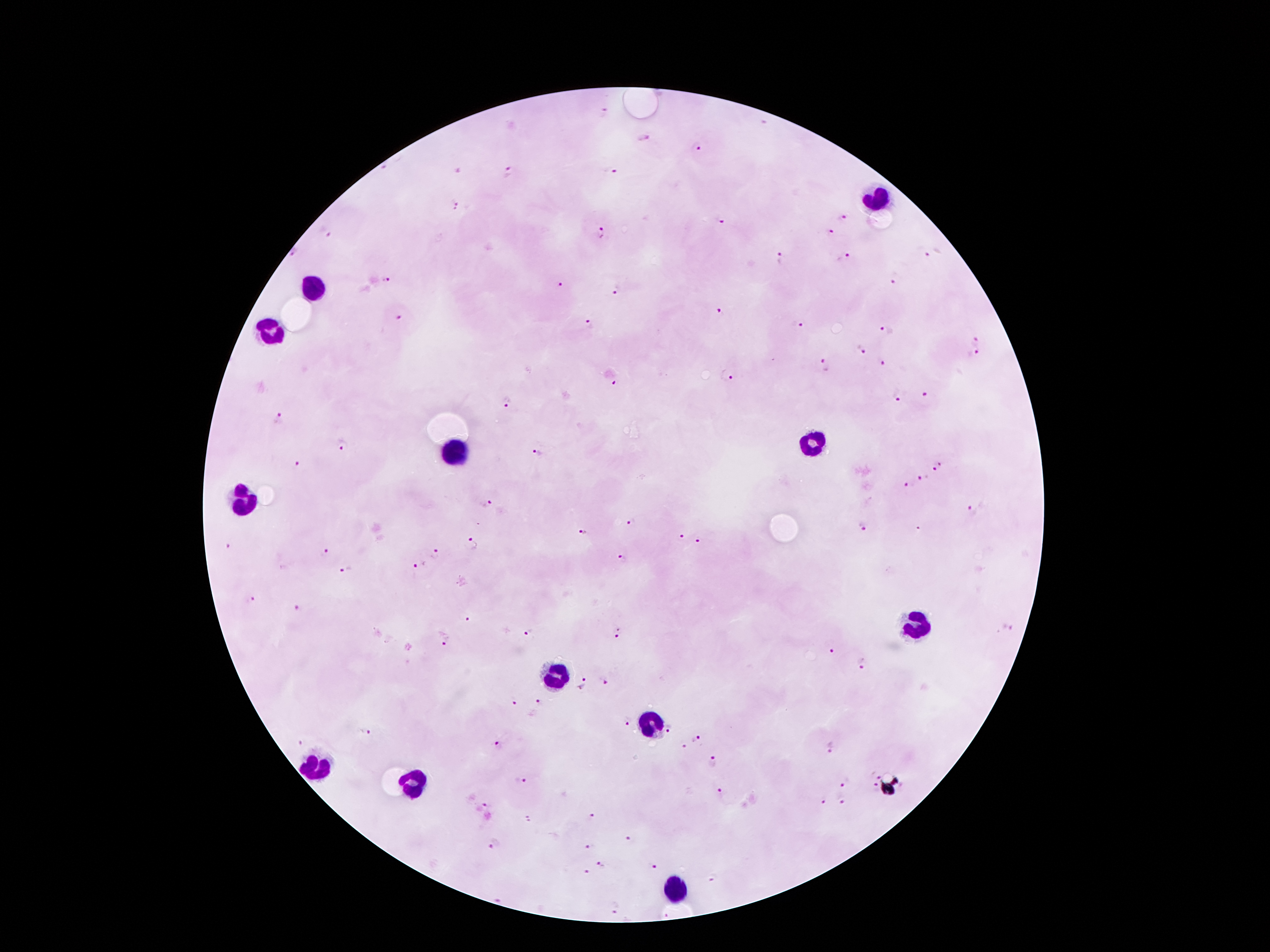
Approximate centers as (x, y) in pixels.
Summary:
  - Malaria parasite locations: (604, 113), (641, 137), (696, 148), (609, 170), (456, 171), (511, 171), (455, 204), (842, 217), (720, 223), (830, 231), (327, 232), (601, 233), (294, 252), (932, 254), (781, 258), (844, 258), (389, 279), (895, 279), (558, 284), (614, 292), (720, 314), (398, 316), (590, 323), (798, 325), (889, 332), (976, 339), (861, 349), (974, 356), (882, 363), (825, 367), (727, 378), (612, 381), (925, 395), (896, 396), (507, 402), (279, 418), (341, 445), (536, 452), (297, 463), (939, 468), (924, 477), (909, 485), (488, 504), (972, 511), (630, 522), (859, 528), (582, 530), (679, 536), (700, 542), (472, 543), (228, 547), (325, 551), (433, 553), (622, 558), (420, 564), (347, 572), (253, 599), (298, 610), (467, 620), (1006, 626), (529, 632), (617, 632), (444, 638), (831, 650), (861, 664), (607, 680), (584, 684), (513, 701), (538, 702), (626, 722), (671, 730), (365, 732), (695, 740), (297, 741), (499, 744), (827, 745), (682, 747), (714, 760), (875, 775), (521, 781), (844, 781), (874, 789), (718, 795), (822, 801), (842, 801), (483, 808), (593, 818), (529, 819), (629, 839), (494, 843), (590, 846), (603, 865), (655, 867), (588, 872), (713, 878), (614, 906)
  - Leukocyte locations: (879, 203), (314, 289), (270, 331), (809, 441), (452, 455), (242, 504), (916, 625), (557, 676), (657, 721), (312, 767), (410, 781), (676, 888)
  - Capture: smartphone through the microscope eyepiece
  - Magnification: 100x
  - Patient malaria status: infected with Plasmodium falciparum
  - Field of view: one from this slide
  - Image size: 1270×952 pixels
  - Stain: Giemsa
  - Preparation: thick blood smear